Give the extent of all Plasmodium vivax-infected red blood cells.
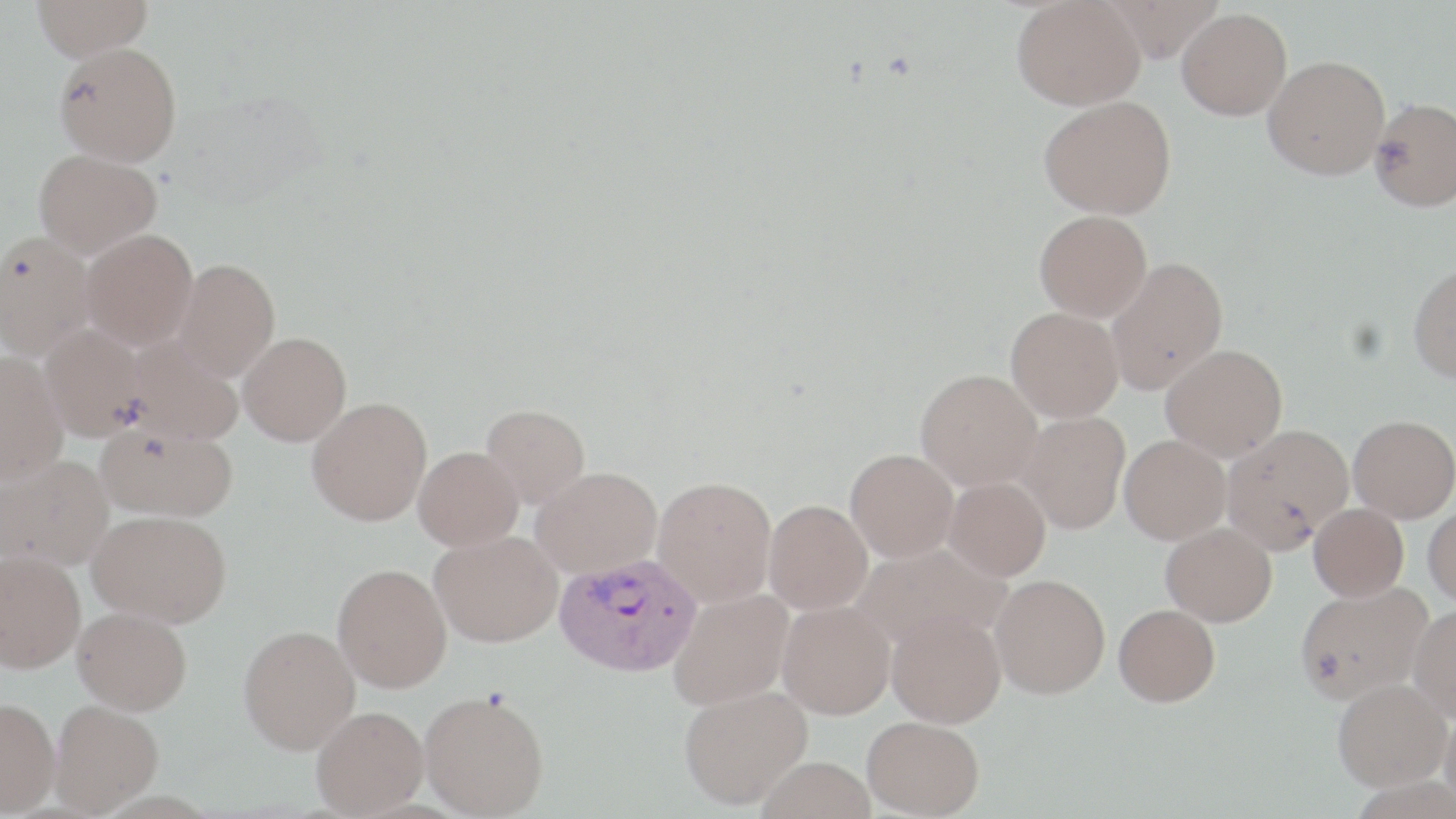
Approximate bounding boxes as (x1,y1)-(x2,y2) corner pairs in pixels.
Plasmodium vivax-infected red blood cells: (554,553)-(702,676).

Uninfected red blood cell locations: (32,0)-(153,60), (1012,0)-(1145,110), (1098,0)-(1224,63), (1176,7)-(1292,120), (54,42)-(182,166), (1263,56)-(1390,179), (1039,96)-(1176,219), (1369,97)-(1456,211), (33,148)-(161,258), (1034,209)-(1152,322), (81,228)-(198,350), (0,232)-(95,359), (1105,257)-(1228,394), (172,258)-(280,380), (1408,262)-(1456,383), (1005,307)-(1124,423), (40,324)-(150,440), (238,331)-(352,445), (125,338)-(243,445), (1161,343)-(1288,460), (0,352)-(68,484), (916,368)-(1042,491), (307,397)-(432,525), (481,403)-(591,507), (1016,411)-(1129,534), (1348,415)-(1456,522), (97,421)-(238,521), (1222,424)-(1355,551), (1119,434)-(1231,544), (413,446)-(524,550), (846,448)-(959,562), (0,455)-(113,569), (531,467)-(663,578), (653,476)-(777,606), (944,476)-(1051,580), (764,500)-(873,614), (1424,501)-(1456,607), (1309,503)-(1409,601), (88,509)-(232,627), (1161,522)-(1277,626), (430,530)-(563,646), (851,542)-(1011,652), (0,550)-(86,673), (333,563)-(452,693), (990,574)-(1110,698), (1295,582)-(1432,704), (669,589)-(794,710), (777,600)-(895,719), (1114,603)-(1220,706), (1409,603)-(1456,720), (73,607)-(192,715), (886,608)-(1006,728), (238,625)-(360,753), (1333,677)-(1452,791), (679,685)-(813,810), (420,688)-(549,818), (0,697)-(59,815), (50,700)-(163,815), (1439,705)-(1456,812), (312,706)-(428,816), (863,715)-(984,817), (756,756)-(875,819). Slide-level diagnosis: Plasmodium vivax. Single field of view. May-Grünwald-Giemsa stain. Image is 1456×819 pixels. Thin blood film. Optical microscopy. 1000x magnification.